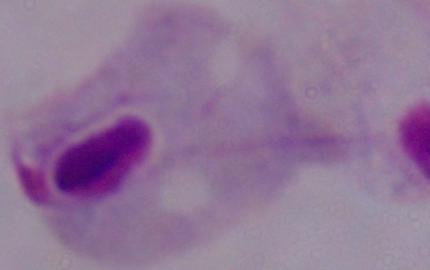
Photomicrograph. 1000x magnification. A trichomonad is shown.